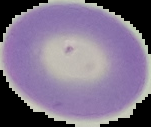

Summary:
  - Preparation: thin blood film
  - Image type: cell region segmented out of the field of view; surrounding area masked to black
  - Result: no malaria parasites seen
  - Image size: 151×127 pixels